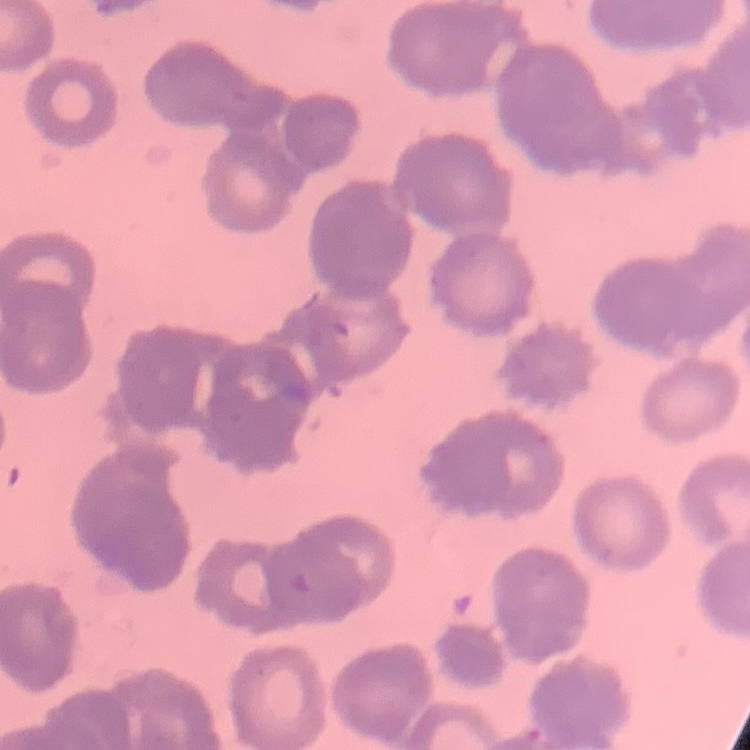

The erythrocytes show rouleaux formation. Stained with either Field's or Giemsa. Thin blood film. Square crop of a larger photomicrograph.